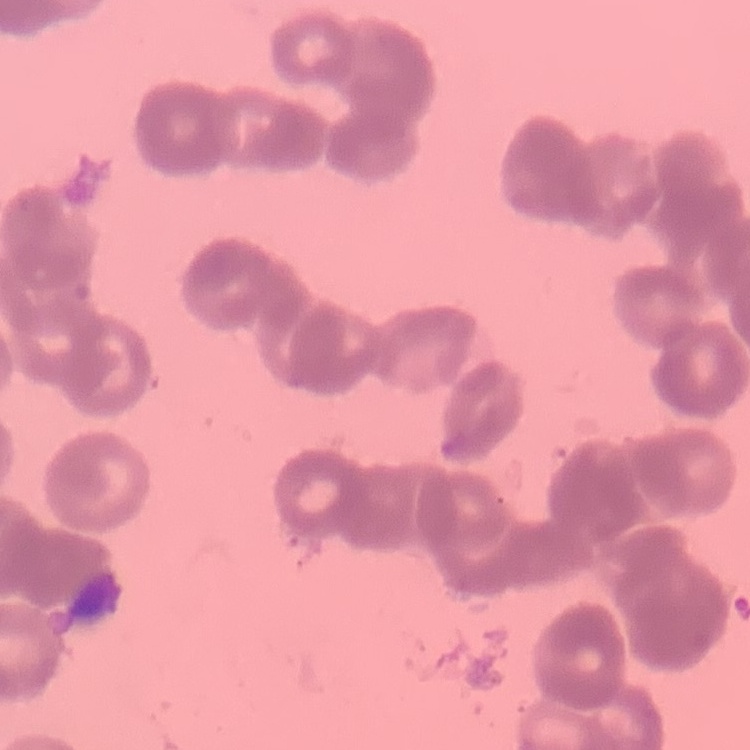

Summary:
  - Erythrocyte morphology: rouleaux formation
  - Image type: square crop of a larger photomicrograph
  - Preparation: thin peripheral smear
  - Stain: Field's or Giemsa